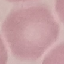
Result: negative for malaria parasites. Giemsa-stained preparation. Photographed with a smartphone camera at the microscope eyepiece. Automatically extracted cell patch, resized to 64 × 64 pixels. Thin smear of blood.